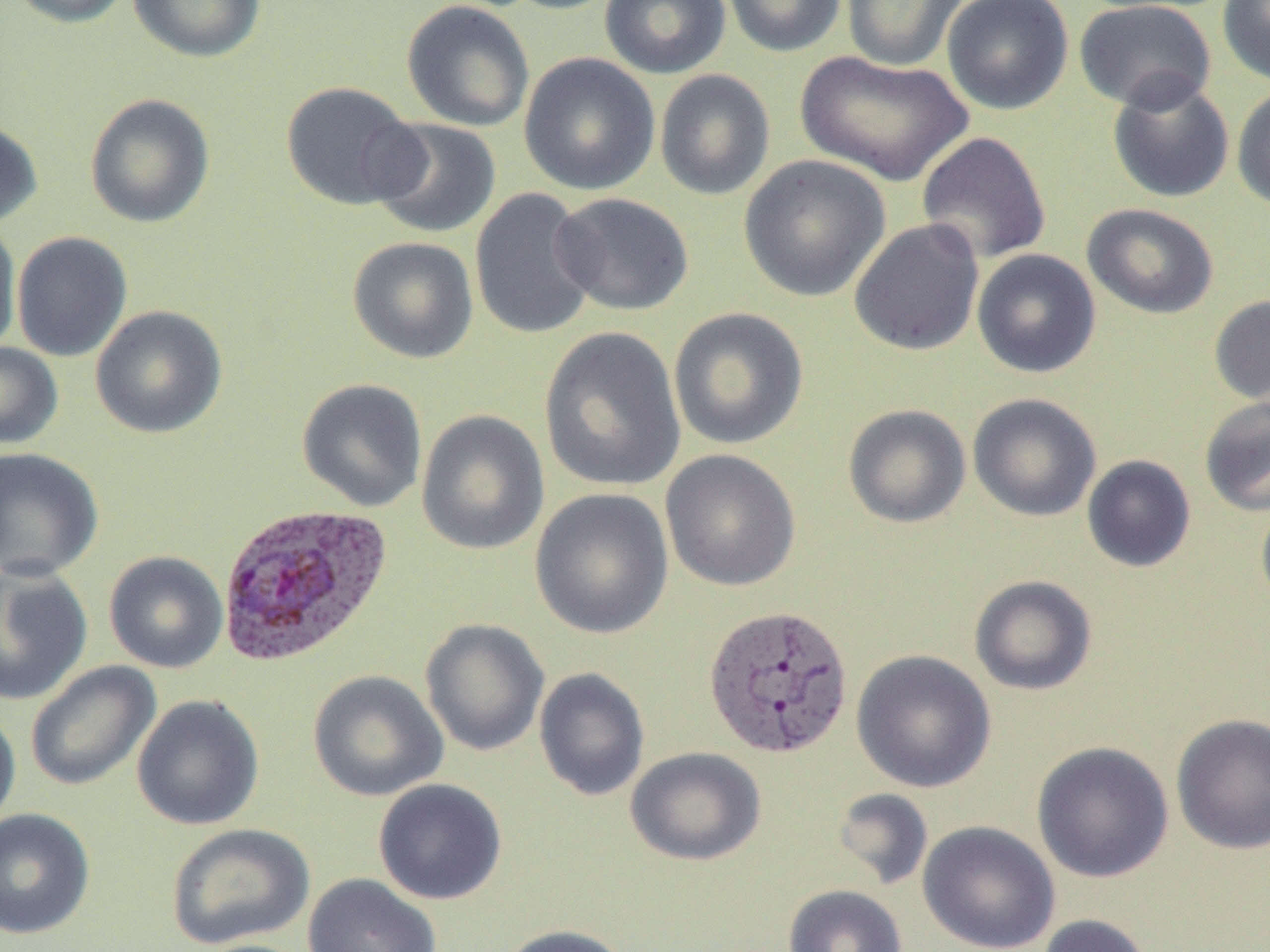 Approximate bounding boxes as named x1/y1/x2/y2 corners in pixels. Uninfected red blood cell locations: (x1=5, y1=0, x2=135, y2=27), (x1=127, y1=0, x2=265, y2=62), (x1=501, y1=0, x2=624, y2=15), (x1=599, y1=0, x2=732, y2=79), (x1=723, y1=0, x2=847, y2=57), (x1=841, y1=0, x2=968, y2=71), (x1=941, y1=0, x2=1074, y2=115), (x1=1073, y1=0, x2=1217, y2=112), (x1=1218, y1=0, x2=1270, y2=87), (x1=401, y1=1, x2=534, y2=132), (x1=795, y1=50, x2=972, y2=187), (x1=518, y1=51, x2=661, y2=195), (x1=654, y1=69, x2=775, y2=201), (x1=1107, y1=75, x2=1235, y2=203), (x1=279, y1=81, x2=424, y2=211), (x1=1231, y1=84, x2=1270, y2=212), (x1=84, y1=93, x2=215, y2=228), (x1=366, y1=117, x2=502, y2=239), (x1=0, y1=119, x2=43, y2=230), (x1=916, y1=131, x2=1052, y2=265), (x1=739, y1=154, x2=890, y2=302), (x1=469, y1=188, x2=598, y2=341), (x1=550, y1=193, x2=695, y2=316), (x1=1081, y1=203, x2=1219, y2=319), (x1=848, y1=219, x2=984, y2=356), (x1=0, y1=220, x2=22, y2=354), (x1=11, y1=231, x2=132, y2=362), (x1=347, y1=236, x2=479, y2=364), (x1=971, y1=249, x2=1101, y2=379), (x1=1209, y1=295, x2=1270, y2=408), (x1=90, y1=305, x2=228, y2=439), (x1=668, y1=307, x2=809, y2=450), (x1=538, y1=325, x2=686, y2=493), (x1=0, y1=342, x2=63, y2=449), (x1=296, y1=378, x2=429, y2=513), (x1=967, y1=393, x2=1102, y2=522), (x1=1199, y1=396, x2=1270, y2=517), (x1=842, y1=403, x2=971, y2=528), (x1=416, y1=409, x2=549, y2=555), (x1=0, y1=447, x2=103, y2=582), (x1=660, y1=449, x2=801, y2=591), (x1=1081, y1=454, x2=1197, y2=573), (x1=529, y1=487, x2=674, y2=639), (x1=1255, y1=493, x2=1270, y2=614), (x1=104, y1=551, x2=228, y2=673), (x1=0, y1=562, x2=93, y2=707), (x1=969, y1=574, x2=1098, y2=696), (x1=420, y1=619, x2=550, y2=757), (x1=851, y1=649, x2=997, y2=793), (x1=25, y1=660, x2=161, y2=791), (x1=534, y1=667, x2=650, y2=801), (x1=308, y1=669, x2=448, y2=801), (x1=131, y1=694, x2=265, y2=831), (x1=0, y1=704, x2=21, y2=835), (x1=1170, y1=712, x2=1270, y2=854), (x1=1031, y1=740, x2=1174, y2=883), (x1=625, y1=747, x2=766, y2=866), (x1=373, y1=778, x2=507, y2=905), (x1=832, y1=787, x2=933, y2=891), (x1=0, y1=808, x2=95, y2=940), (x1=917, y1=820, x2=1060, y2=952), (x1=166, y1=823, x2=315, y2=950), (x1=302, y1=873, x2=442, y2=952), (x1=783, y1=884, x2=907, y2=952), (x1=1036, y1=913, x2=1155, y2=952), (x1=495, y1=923, x2=634, y2=952), (x1=187, y1=938, x2=317, y2=952). Plasmodium vivax-infected red blood cell locations: (x1=216, y1=501, x2=394, y2=667), (x1=702, y1=602, x2=855, y2=760). Slide-level diagnosis: Plasmodium vivax. Optical microscopy. 1000x magnification. Image is 1270×952 pixels. Thin blood smear. Single field of view.